Comment on the morphology of the red blood cells.
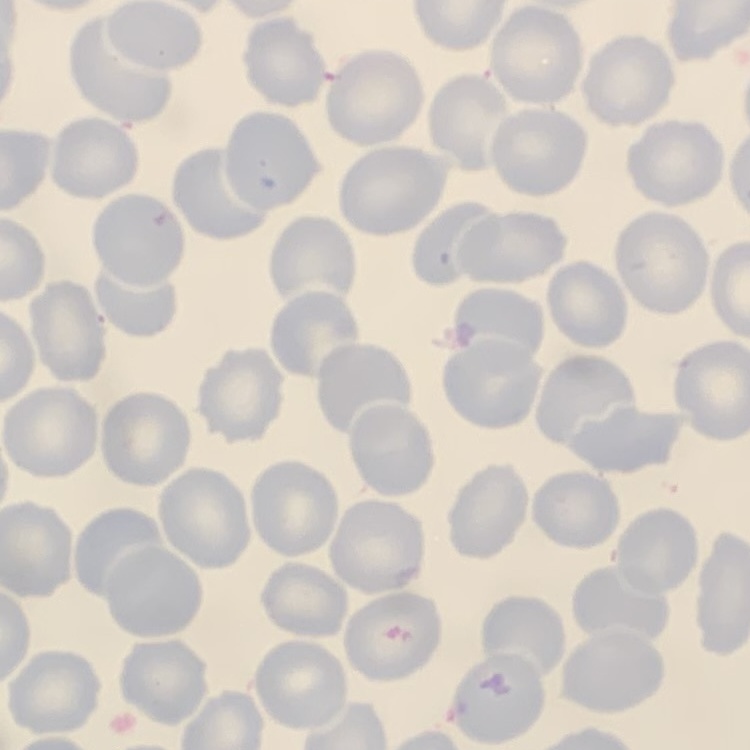

They show no rouleaux formation.

Square crop of a larger photomicrograph. Thin blood film. Field's or Giemsa stain.